Assess this cell for malaria.
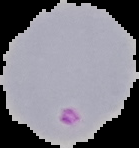
It is parasitized.

preparation = thin blood smear
image type = segmented cell region on a black background
image size = 139×148 pixels